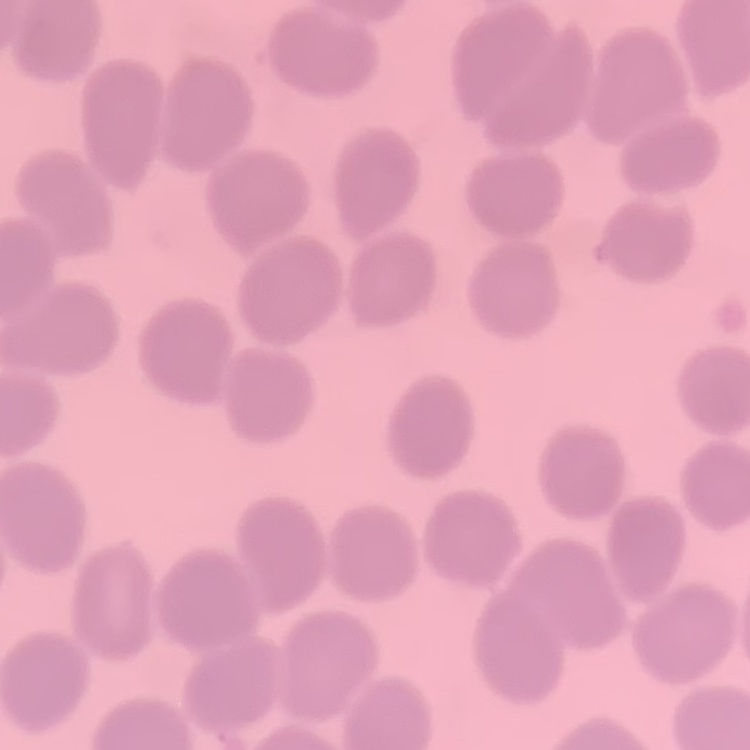

erythrocyte morphology = no rouleaux formation
stain = Field's or Giemsa
preparation = thin peripheral smear
image type = one tile cut from a larger photomicrograph